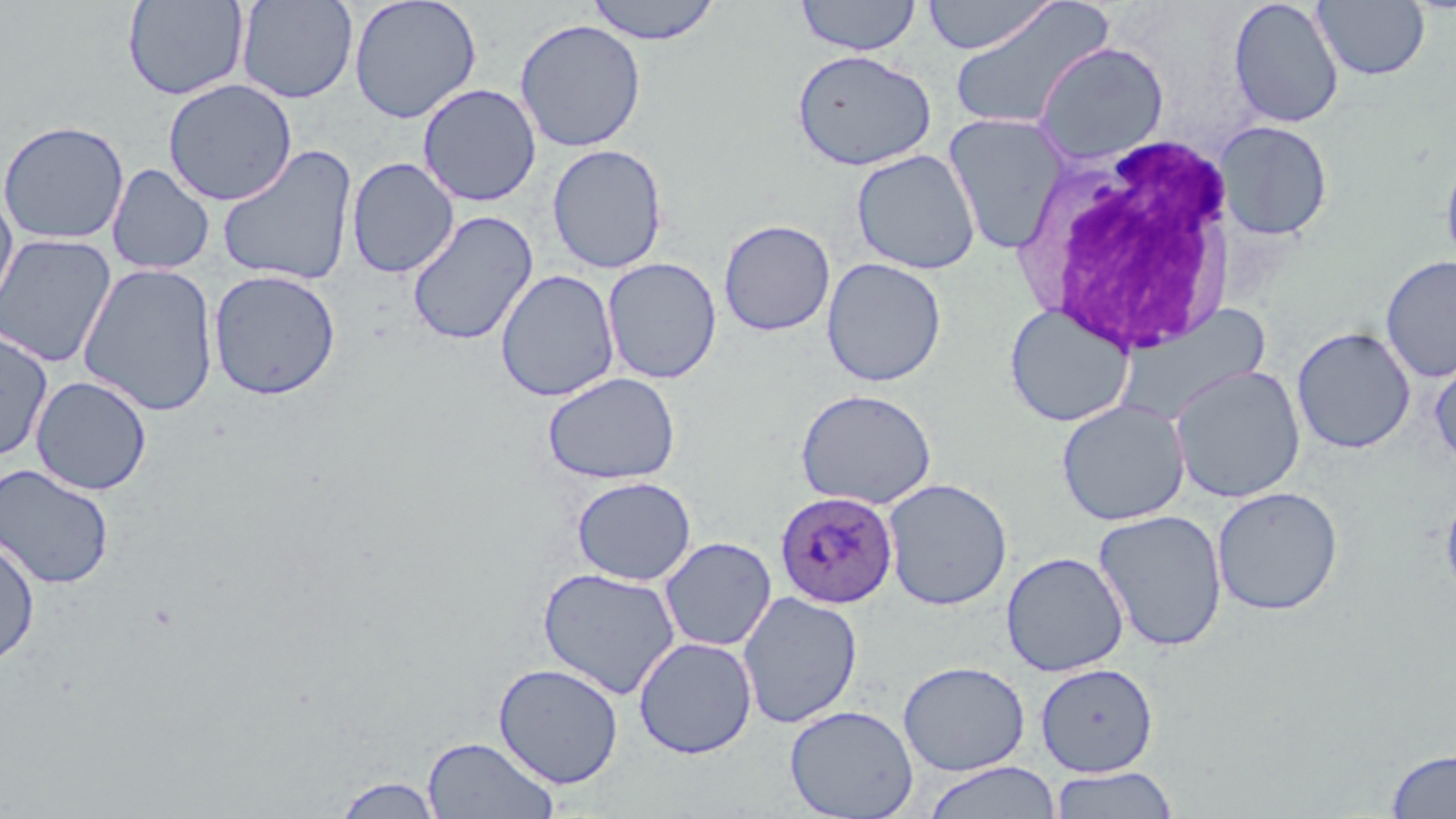

{
  "slide_level_diagnosis": "Plasmodium ovale",
  "image_size": "1456×819 pixels",
  "stain": "May-Grünwald-Giemsa",
  "modality": "optical microscopy",
  "uninfected_red_blood_cell_locations": "approximate bounding boxes as (x1,y1)-(x2,y2) corner pairs in pixels: (122,0)-(250,101), (236,0)-(358,104), (348,0)-(483,124), (585,0)-(722,45), (795,0)-(922,56), (921,0)-(1058,54), (1228,0)-(1344,129), (947,1)-(1115,133), (1313,1)-(1429,81), (514,18)-(646,152), (1033,41)-(1169,165), (791,48)-(937,171), (162,78)-(297,206), (417,83)-(542,207), (942,113)-(1070,255), (0,120)-(129,245), (1215,120)-(1333,240), (547,143)-(668,274), (217,144)-(357,286), (1440,147)-(1456,276), (851,149)-(981,275), (347,157)-(459,278), (107,163)-(214,276), (0,187)-(18,321), (406,211)-(538,346), (718,219)-(836,336), (0,233)-(118,368), (1380,256)-(1456,382), (602,257)-(723,384), (821,257)-(947,387), (77,263)-(219,417), (208,269)-(341,400), (496,269)-(620,402), (1003,303)-(1134,427), (1111,305)-(1272,428), (1292,326)-(1416,454), (0,328)-(53,461), (1429,353)-(1456,471), (1170,364)-(1306,503), (542,371)-(680,484), (30,375)-(152,495), (795,388)-(937,510), (1056,399)-(1190,526), (0,463)-(115,589), (571,476)-(697,585), (882,477)-(1013,611), (1211,486)-(1344,615), (1440,486)-(1456,606), (1093,509)-(1229,652), (659,536)-(777,652), (0,537)-(40,666), (1001,551)-(1129,676), (537,566)-(681,700), (737,591)-(863,728), (633,636)-(758,759), (898,660)-(1031,776), (493,662)-(624,789), (1034,663)-(1158,777), (785,704)-(919,819), (422,736)-(559,819), (1385,747)-(1456,818), (922,761)-(1062,819), (1049,766)-(1180,819), (333,775)-(445,818)",
  "field_of_view": "single",
  "white_blood_cell_locations": "approximate bounding boxes as (x1,y1)-(x2,y2) corner pairs in pixels: (1019,133)-(1243,356)",
  "magnification": "1000x",
  "preparation": "thin blood smear",
  "plasmodium_ovale_infected_red_blood_cell_locations": "approximate bounding boxes as (x1,y1)-(x2,y2) corner pairs in pixels: (775,490)-(898,608)"
}